Name the cell type shown.
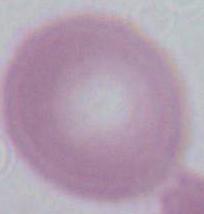

An erythrocyte.

modality = micrograph
magnification = 1000x